Identify the parasite.
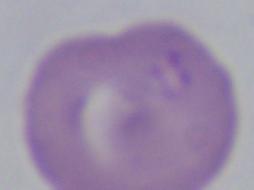

This is Babesia.

Summary:
  - Magnification: 1000x
  - Modality: micrograph